Outline each uninfected red blood cell.
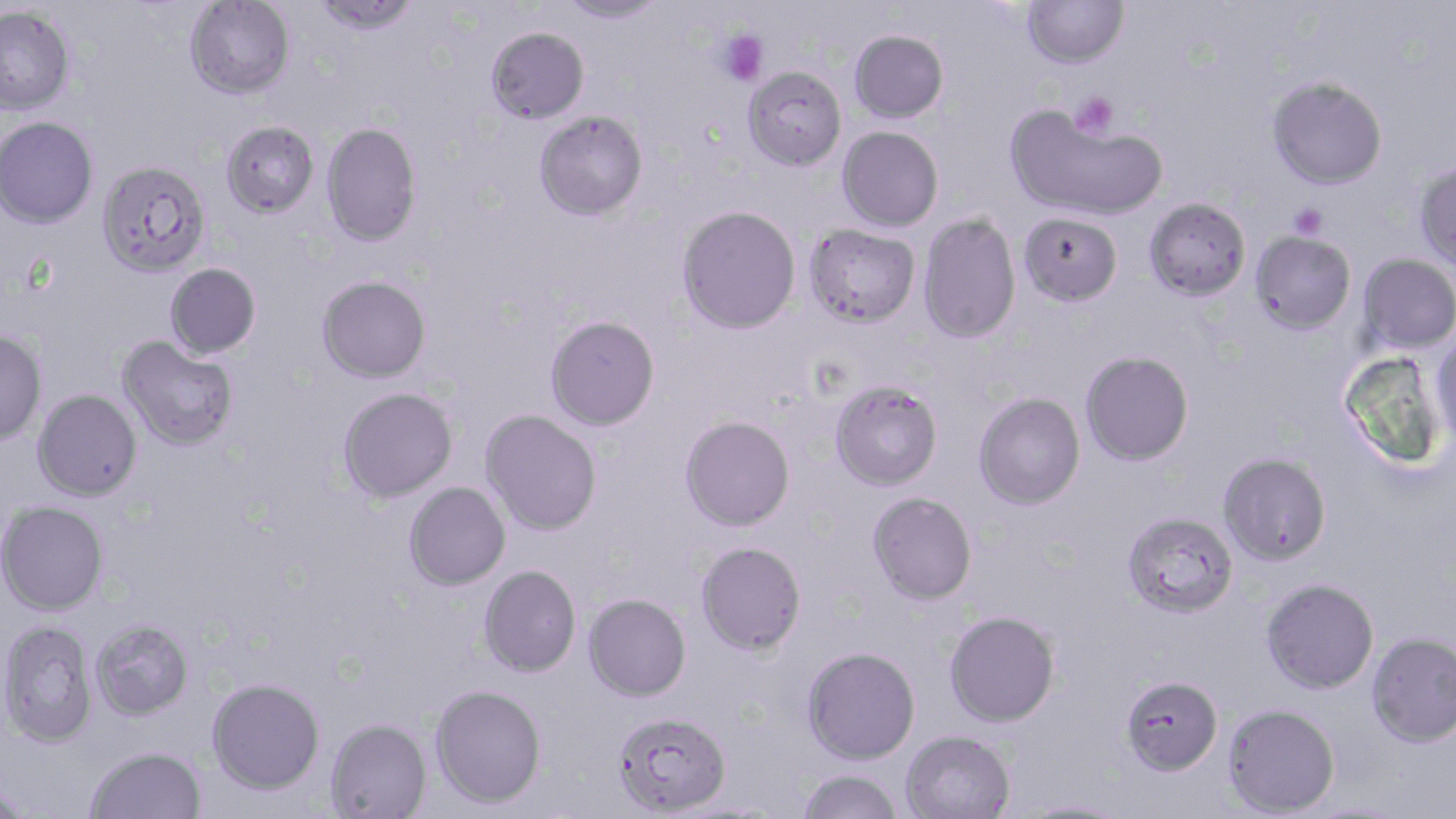

Approximate bounding boxes as (x1, y1, x2, y2) in pixels.
Uninfected red blood cells: (311, 0, 421, 36), (557, 0, 669, 25), (1021, 0, 1129, 68), (184, 1, 295, 100), (0, 6, 74, 115), (486, 27, 590, 123), (849, 29, 949, 123), (743, 65, 847, 171), (1267, 76, 1387, 189), (1006, 105, 1168, 222), (534, 110, 648, 221), (0, 116, 98, 228), (221, 120, 319, 219), (321, 122, 422, 247), (837, 126, 943, 232), (97, 160, 211, 277), (1413, 160, 1456, 272), (1144, 197, 1251, 302), (677, 205, 801, 335), (1018, 212, 1122, 306), (918, 213, 1021, 344), (803, 224, 920, 329), (1250, 231, 1356, 336), (1358, 254, 1456, 355), (165, 263, 261, 359), (316, 275, 431, 383), (545, 315, 660, 430), (1430, 326, 1456, 446), (0, 329, 47, 445), (117, 336, 240, 452), (1080, 350, 1194, 466), (829, 380, 943, 490), (337, 387, 458, 503), (32, 389, 142, 501), (973, 392, 1085, 510), (480, 410, 602, 536), (679, 415, 795, 531), (1217, 452, 1332, 566), (404, 482, 510, 590), (866, 492, 977, 605), (0, 501, 109, 616), (1121, 510, 1238, 618), (695, 541, 807, 656), (478, 565, 581, 677), (1260, 578, 1379, 694), (583, 593, 691, 701), (944, 610, 1060, 727), (0, 619, 97, 748), (90, 619, 194, 720), (1366, 631, 1456, 747), (801, 646, 920, 764), (1120, 675, 1223, 775), (206, 678, 325, 795), (430, 684, 547, 807), (1222, 703, 1340, 817), (612, 710, 731, 816), (325, 719, 432, 819), (900, 730, 1016, 819), (86, 746, 206, 819), (796, 769, 903, 819), (1, 786, 34, 817), (1014, 798, 1129, 818).

Summary:
  - Platelet locations: (718, 30, 769, 88), (1070, 91, 1118, 140), (1290, 203, 1327, 238)
  - Slide-level diagnosis: Plasmodium falciparum
  - Preparation: thin blood smear
  - Field of view: one of a larger specimen
  - Image size: 1456×819 pixels
  - Stain: May-Grünwald-Giemsa
  - Modality: optical microscopy
  - Magnification: 1000x